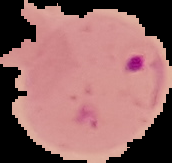

image type = segmented cell region with the area outside set to black
image size = 172×163 pixels
result = malaria parasites detected
preparation = thin blood film